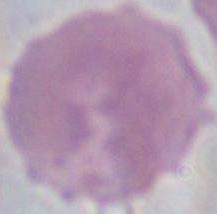
Summary:
  - Identification: red blood cell
  - Magnification: 1000x
  - Modality: photomicrograph